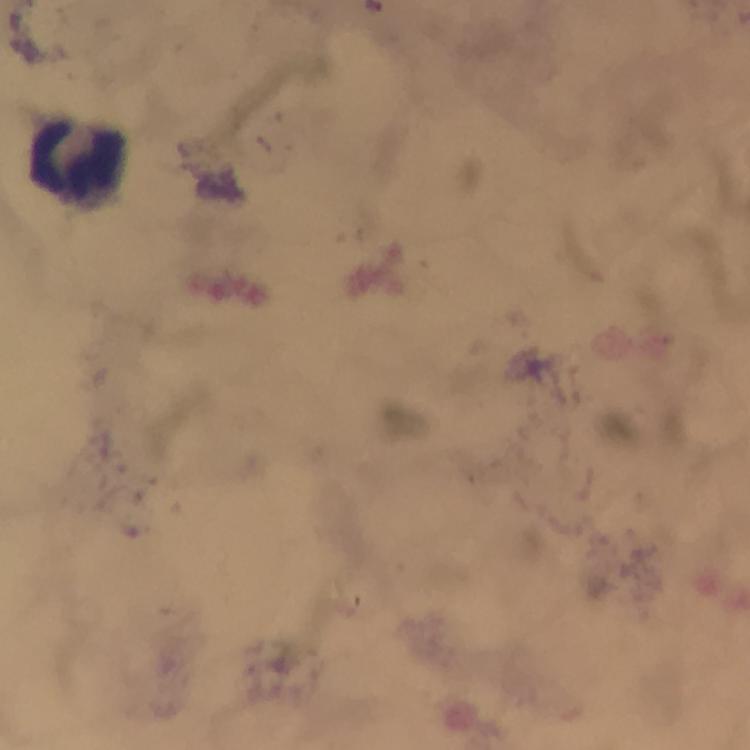
Approximate object centers, in pixels from the top-left corner.
Summary:
  - Leukocyte locations: (x=82, y=164)
  - Immersion oil: applied
  - Plasmodium parasites: none seen
  - Capture: smartphone camera through the microscope
  - Context: from a malaria diagnostic workup
  - Stain: Giemsa
  - Image size: 750×750 pixels
  - Cropped from: a single field of view
  - Magnification: 100x
  - Preparation: thick blood smear